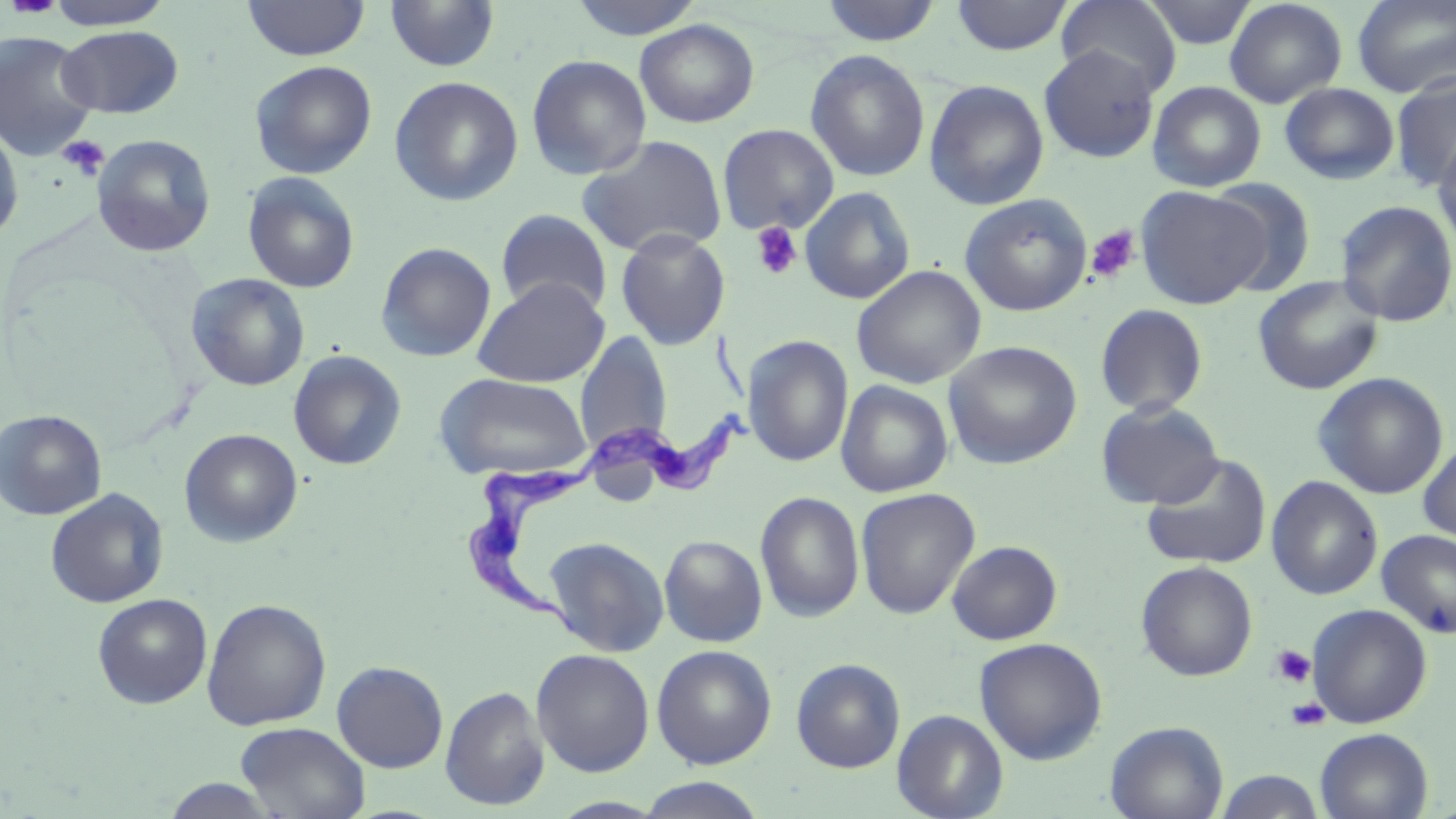 Approximate bounding boxes as [x1, y1, x2, y2] in pixels. Uninfected red blood cell locations: [44, 0, 174, 29], [243, 0, 370, 61], [385, 0, 500, 73], [566, 0, 707, 40], [950, 0, 1074, 56], [1056, 0, 1182, 96], [1142, 0, 1257, 49], [1224, 0, 1348, 108], [1352, 0, 1456, 97], [818, 1, 943, 46], [634, 19, 760, 128], [56, 25, 183, 118], [1, 31, 99, 161], [1039, 45, 1160, 163], [805, 49, 930, 182], [525, 54, 652, 180], [249, 60, 377, 179], [1390, 73, 1456, 190], [389, 76, 524, 206], [924, 79, 1049, 211], [1147, 81, 1266, 192], [1279, 82, 1400, 185], [0, 120, 24, 244], [717, 123, 840, 235], [1432, 131, 1456, 254], [92, 134, 216, 256], [576, 134, 728, 258], [242, 171, 360, 293], [1205, 179, 1317, 295], [799, 186, 916, 305], [1136, 186, 1270, 309], [959, 193, 1093, 316], [1335, 200, 1456, 327], [495, 209, 613, 317], [615, 229, 730, 350], [375, 241, 497, 362], [851, 265, 986, 389], [186, 272, 311, 391], [1253, 275, 1384, 395], [472, 277, 610, 387], [1095, 304, 1209, 416], [575, 330, 671, 456], [742, 335, 854, 466], [943, 340, 1082, 469], [288, 349, 407, 470], [1312, 372, 1449, 499], [434, 373, 594, 479], [835, 379, 954, 497], [1096, 400, 1224, 509], [0, 409, 107, 520], [179, 428, 303, 547], [1418, 437, 1456, 550], [1141, 454, 1272, 570], [1266, 476, 1383, 600], [855, 487, 980, 620], [45, 488, 168, 608], [754, 491, 865, 623], [1376, 529, 1456, 639], [658, 534, 768, 647], [543, 536, 670, 656], [946, 540, 1063, 645], [1135, 560, 1258, 681], [92, 593, 212, 709], [202, 598, 332, 730], [1307, 604, 1432, 728], [974, 636, 1108, 765], [651, 645, 777, 769], [531, 648, 655, 777], [791, 658, 905, 773], [332, 660, 448, 773], [440, 685, 550, 810], [892, 709, 1009, 819], [1105, 721, 1229, 819], [236, 722, 370, 819], [1315, 728, 1432, 819], [1214, 770, 1327, 818], [636, 777, 767, 817], [160, 778, 283, 818], [550, 797, 667, 818]. Trypanosoma brucei locations: [573, 330, 776, 500], [460, 456, 591, 643]. Platelet locations: [57, 135, 109, 181], [750, 221, 802, 281], [1085, 226, 1140, 283], [1270, 644, 1317, 688], [1286, 698, 1331, 731]. Slide-level diagnosis: Trypanosoma brucei. Thin blood smear. May-Grünwald-Giemsa-stained preparation. Light microscopy. Image is 1456×819 pixels. One field of a larger specimen. 1000x magnification.